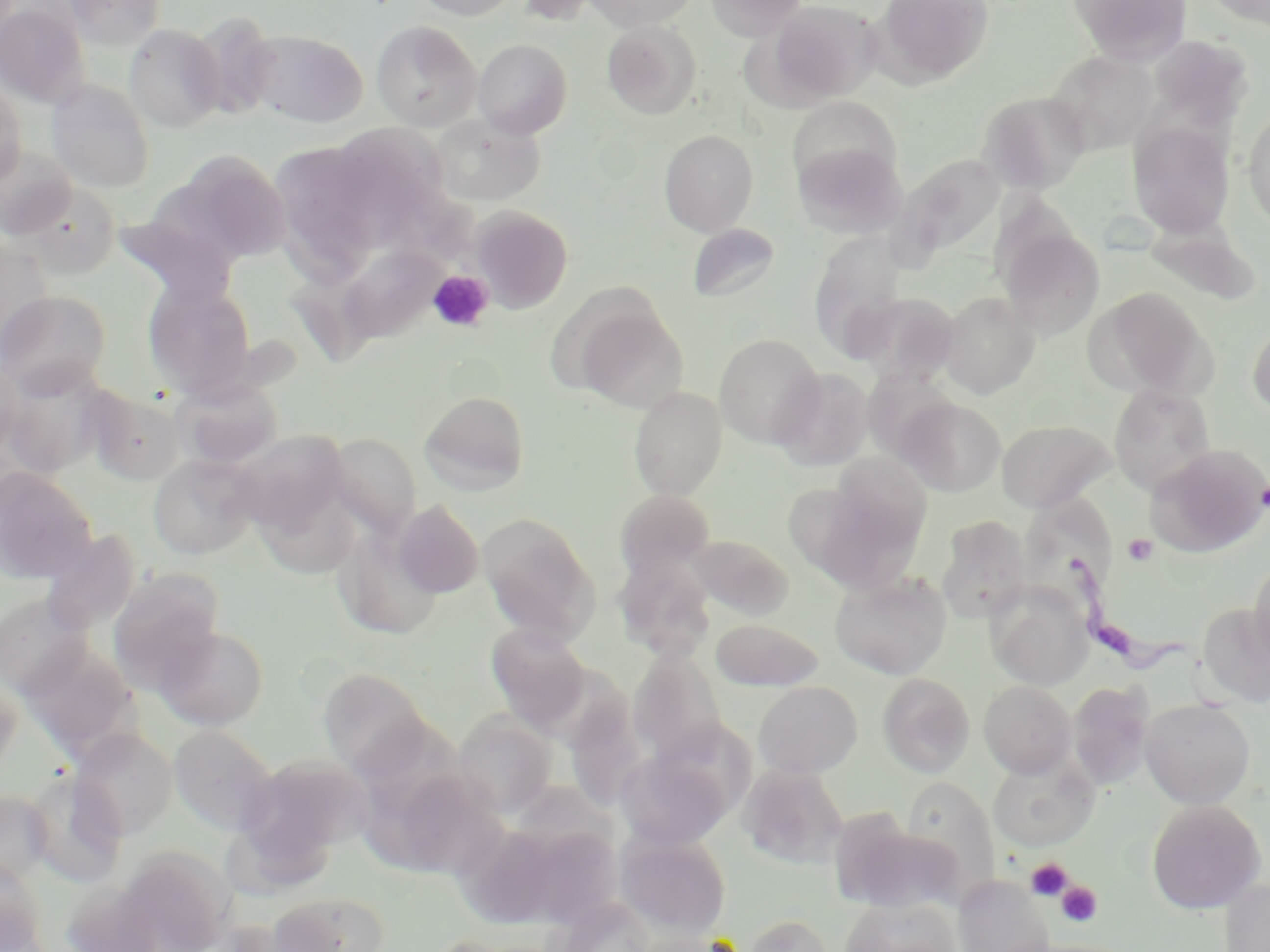
Summary:
  - Coordinate format: approximate bounding boxes as named x1/y1/x2/y2 corners in pixels
  - Trypanosoma brucei locations: (x1=1062, y1=556, x2=1216, y2=691)
  - Platelet locations: (x1=428, y1=270, x2=494, y2=333), (x1=1255, y1=479, x2=1270, y2=511), (x1=1122, y1=534, x2=1159, y2=566), (x1=1025, y1=857, x2=1073, y2=901), (x1=1056, y1=882, x2=1103, y2=927)
  - Uninfected red blood cell locations: (x1=63, y1=0, x2=167, y2=50), (x1=412, y1=0, x2=522, y2=20), (x1=583, y1=0, x2=699, y2=31), (x1=704, y1=0, x2=808, y2=39), (x1=764, y1=0, x2=883, y2=104), (x1=874, y1=0, x2=993, y2=87), (x1=1068, y1=0, x2=1193, y2=65), (x1=0, y1=1, x2=91, y2=109), (x1=192, y1=14, x2=281, y2=121), (x1=602, y1=20, x2=702, y2=120), (x1=371, y1=21, x2=481, y2=132), (x1=124, y1=24, x2=225, y2=132), (x1=247, y1=29, x2=368, y2=127), (x1=1146, y1=35, x2=1254, y2=131), (x1=473, y1=38, x2=573, y2=138), (x1=1045, y1=50, x2=1158, y2=155), (x1=0, y1=78, x2=27, y2=187), (x1=46, y1=79, x2=156, y2=193), (x1=978, y1=90, x2=1091, y2=194), (x1=787, y1=97, x2=901, y2=192), (x1=1242, y1=109, x2=1270, y2=228), (x1=428, y1=114, x2=546, y2=207), (x1=1127, y1=122, x2=1235, y2=238), (x1=659, y1=128, x2=759, y2=237), (x1=346, y1=129, x2=461, y2=218), (x1=793, y1=141, x2=905, y2=239), (x1=0, y1=145, x2=79, y2=241), (x1=269, y1=146, x2=378, y2=241), (x1=172, y1=150, x2=294, y2=266), (x1=895, y1=153, x2=1006, y2=260), (x1=469, y1=205, x2=573, y2=313), (x1=1143, y1=221, x2=1259, y2=304), (x1=687, y1=223, x2=781, y2=302), (x1=999, y1=227, x2=1104, y2=340), (x1=330, y1=238, x2=450, y2=353), (x1=0, y1=240, x2=56, y2=358), (x1=812, y1=247, x2=919, y2=361), (x1=143, y1=276, x2=257, y2=399), (x1=1086, y1=286, x2=1215, y2=399), (x1=0, y1=290, x2=111, y2=398), (x1=939, y1=290, x2=1040, y2=398), (x1=853, y1=292, x2=960, y2=385), (x1=567, y1=299, x2=690, y2=413), (x1=1247, y1=315, x2=1270, y2=418), (x1=714, y1=333, x2=824, y2=448), (x1=0, y1=359, x2=24, y2=466), (x1=1, y1=361, x2=108, y2=478), (x1=774, y1=367, x2=873, y2=471), (x1=861, y1=368, x2=957, y2=462), (x1=172, y1=375, x2=284, y2=469), (x1=1109, y1=384, x2=1216, y2=492), (x1=87, y1=387, x2=186, y2=486), (x1=628, y1=387, x2=727, y2=499), (x1=419, y1=390, x2=530, y2=496), (x1=897, y1=396, x2=1007, y2=496), (x1=997, y1=419, x2=1113, y2=512), (x1=228, y1=430, x2=351, y2=535), (x1=324, y1=433, x2=422, y2=538), (x1=1147, y1=445, x2=1270, y2=556), (x1=148, y1=453, x2=260, y2=560), (x1=796, y1=467, x2=931, y2=591), (x1=0, y1=468, x2=97, y2=582), (x1=614, y1=489, x2=716, y2=579), (x1=1033, y1=497, x2=1122, y2=587), (x1=393, y1=501, x2=484, y2=598), (x1=477, y1=512, x2=600, y2=644), (x1=936, y1=514, x2=1032, y2=623), (x1=331, y1=525, x2=444, y2=639), (x1=40, y1=529, x2=141, y2=634), (x1=685, y1=534, x2=794, y2=620), (x1=615, y1=552, x2=716, y2=659), (x1=1248, y1=555, x2=1270, y2=671), (x1=107, y1=567, x2=225, y2=688), (x1=830, y1=570, x2=952, y2=679), (x1=985, y1=580, x2=1094, y2=689), (x1=0, y1=593, x2=93, y2=699), (x1=1197, y1=602, x2=1270, y2=708), (x1=710, y1=617, x2=825, y2=692), (x1=154, y1=624, x2=269, y2=730), (x1=485, y1=624, x2=592, y2=729), (x1=19, y1=642, x2=141, y2=760), (x1=627, y1=648, x2=730, y2=765), (x1=317, y1=668, x2=432, y2=776), (x1=0, y1=673, x2=22, y2=777), (x1=877, y1=673, x2=974, y2=777), (x1=979, y1=680, x2=1077, y2=777), (x1=754, y1=681, x2=862, y2=778), (x1=1068, y1=682, x2=1154, y2=789), (x1=570, y1=686, x2=650, y2=802), (x1=1140, y1=698, x2=1255, y2=809), (x1=453, y1=711, x2=558, y2=818), (x1=169, y1=725, x2=278, y2=836), (x1=70, y1=728, x2=178, y2=839), (x1=616, y1=747, x2=733, y2=850), (x1=238, y1=753, x2=373, y2=866), (x1=988, y1=754, x2=1098, y2=851), (x1=739, y1=764, x2=849, y2=868), (x1=408, y1=768, x2=512, y2=883), (x1=23, y1=769, x2=127, y2=887), (x1=901, y1=777, x2=1000, y2=894), (x1=0, y1=789, x2=53, y2=884), (x1=1147, y1=800, x2=1266, y2=914), (x1=838, y1=818, x2=962, y2=915), (x1=462, y1=819, x2=618, y2=931), (x1=615, y1=830, x2=731, y2=940), (x1=116, y1=846, x2=235, y2=952), (x1=0, y1=857, x2=49, y2=950), (x1=953, y1=875, x2=1055, y2=952), (x1=1220, y1=877, x2=1270, y2=952), (x1=268, y1=891, x2=390, y2=952), (x1=839, y1=896, x2=962, y2=952), (x1=552, y1=897, x2=657, y2=951), (x1=740, y1=913, x2=834, y2=952)
  - Slide-level diagnosis: Trypanosoma brucei
  - Modality: light microscopy
  - Stain: May-Grünwald-Giemsa
  - Magnification: 1000x
  - Preparation: thin blood smear
  - Image size: 1270×952 pixels
  - Field of view: one of a larger specimen